State which parasite is depicted.
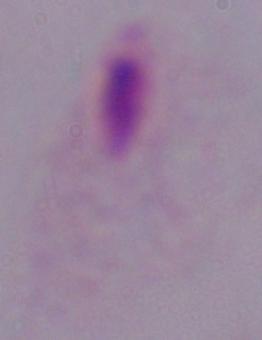

This is a trichomonad.

Micrograph. 1000x magnification.